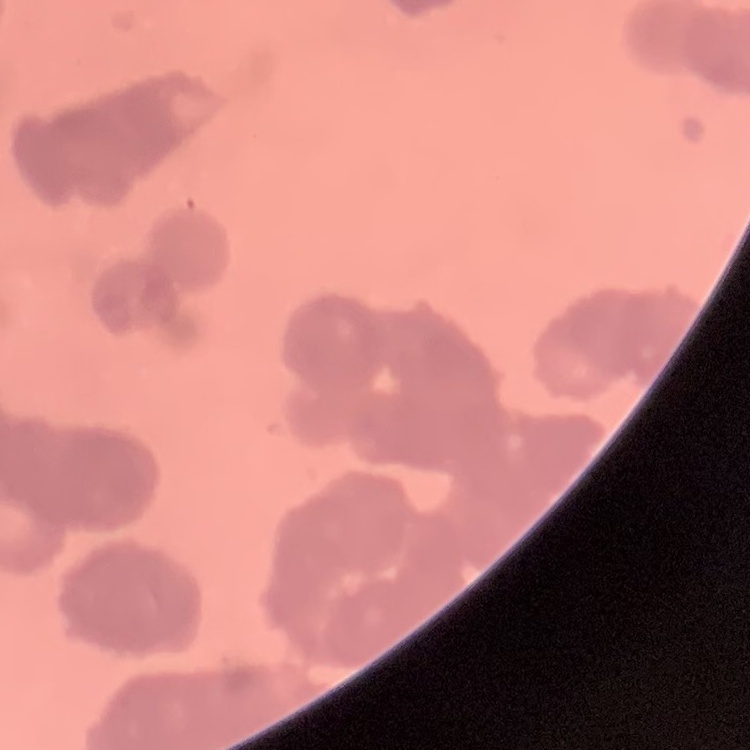

erythrocyte morphology = rouleaux formation
stain = Field's or Giemsa
image type = one tile cut from a larger photomicrograph
preparation = thin blood smear